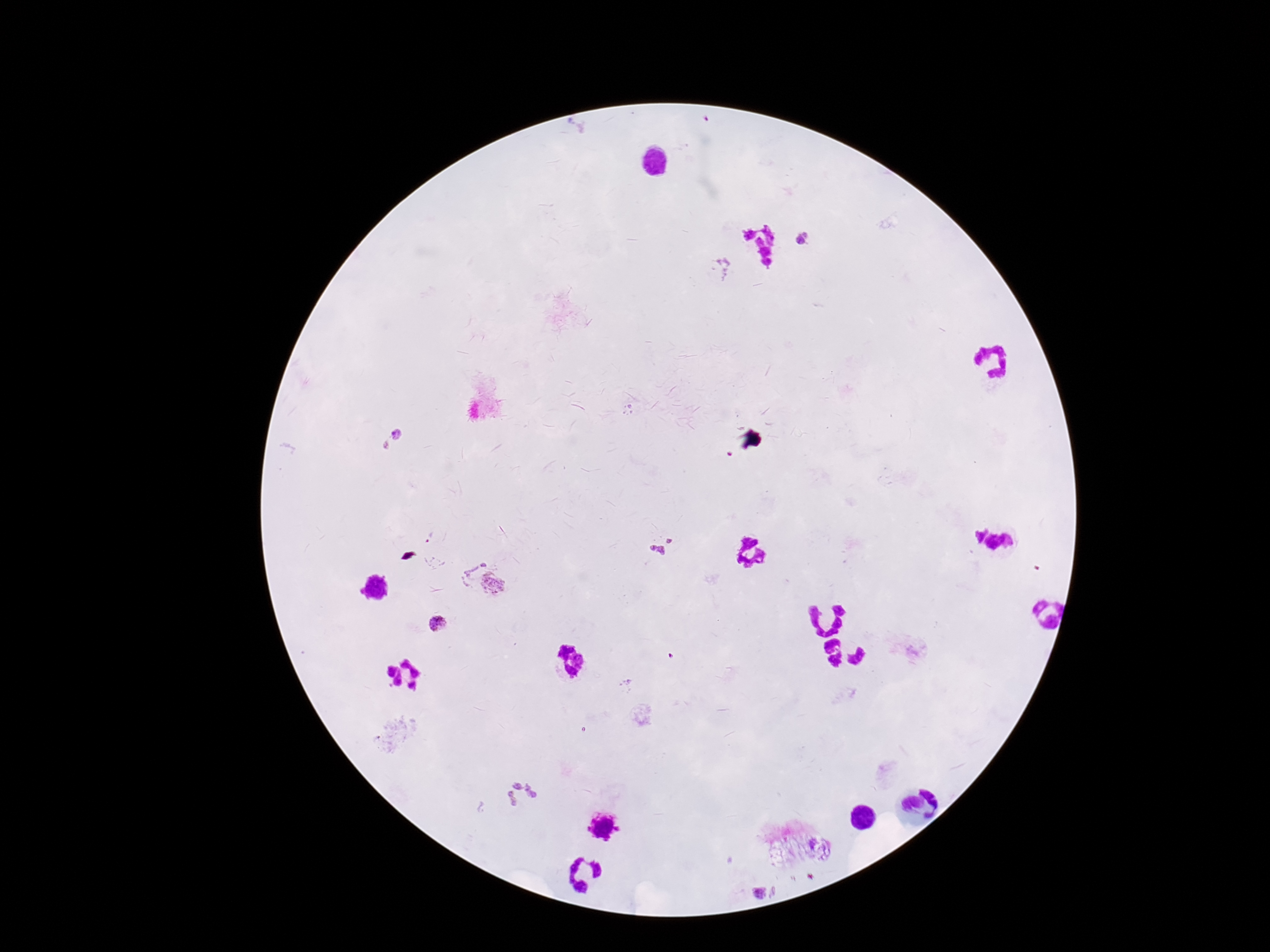

Approximate object centers, in pixels from the top-left corner. Plasmodium parasite locations: (x=804, y=237), (x=720, y=269), (x=392, y=439), (x=661, y=545), (x=474, y=577), (x=497, y=584), (x=434, y=624), (x=518, y=792), (x=759, y=891). Photographed through the microscope eyepiece with a smartphone camera. Patient malaria status: positive. 100x magnification. Single field of view. Image is 1270×952 pixels. Thick blood film. Giemsa-stained preparation.